Comment on the morphology of the erythrocytes.
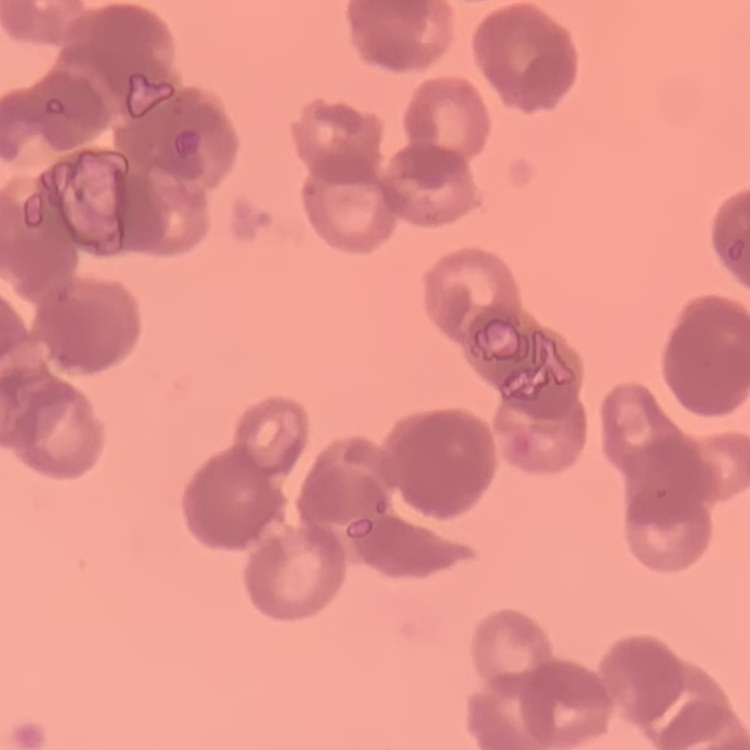

They show rouleaux formation.

Summary:
  - Stain: Field's or Giemsa
  - Image type: one tile cut from a larger photomicrograph
  - Preparation: thin blood smear